Locate malaria parasites and leukocytes.
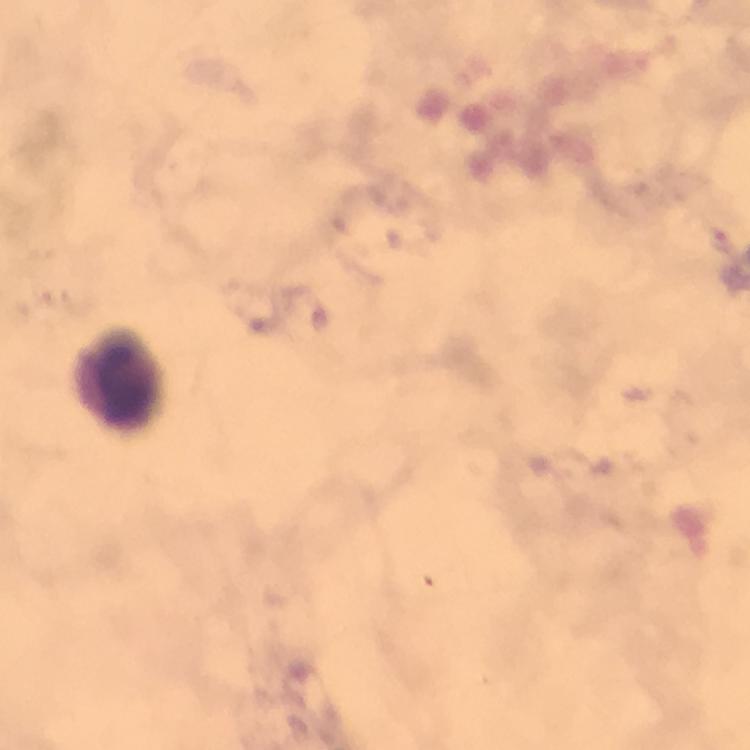
No malaria parasites seen.
Approximate centers as [x, y] in pixels.
Leukocytes: [118, 377].

Cropped region of a single field of view. Thick blood smear. Photographed with a smartphone mounted on the microscope. 100x magnification. Immersion oil was used. From a malaria diagnostic workup. Image is 750×750 pixels. Giemsa-stained preparation.